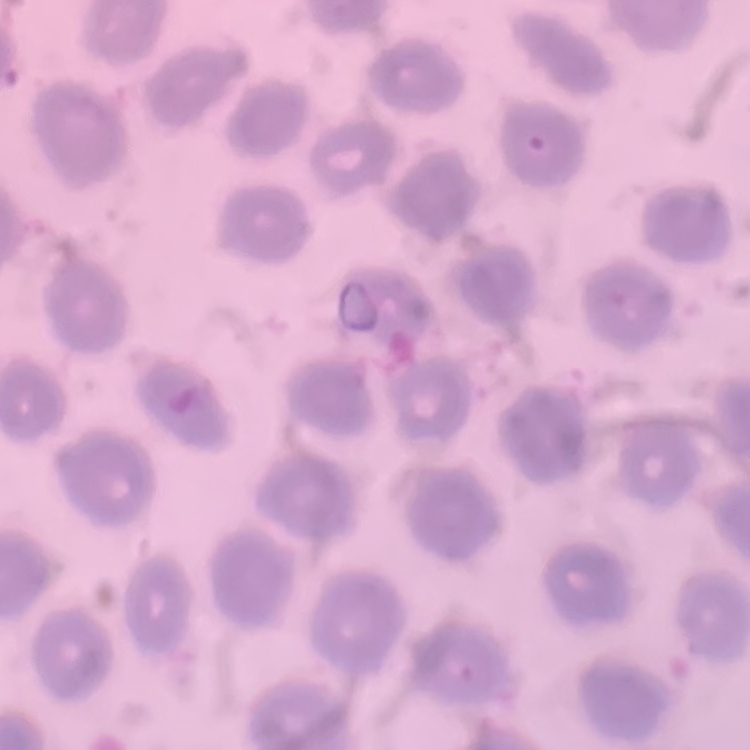
red blood cell morphology = no rouleaux formation
preparation = thin blood smear
image type = one tile cut from a larger photomicrograph
stain = Field's or Giemsa